Point out each malaria parasite.
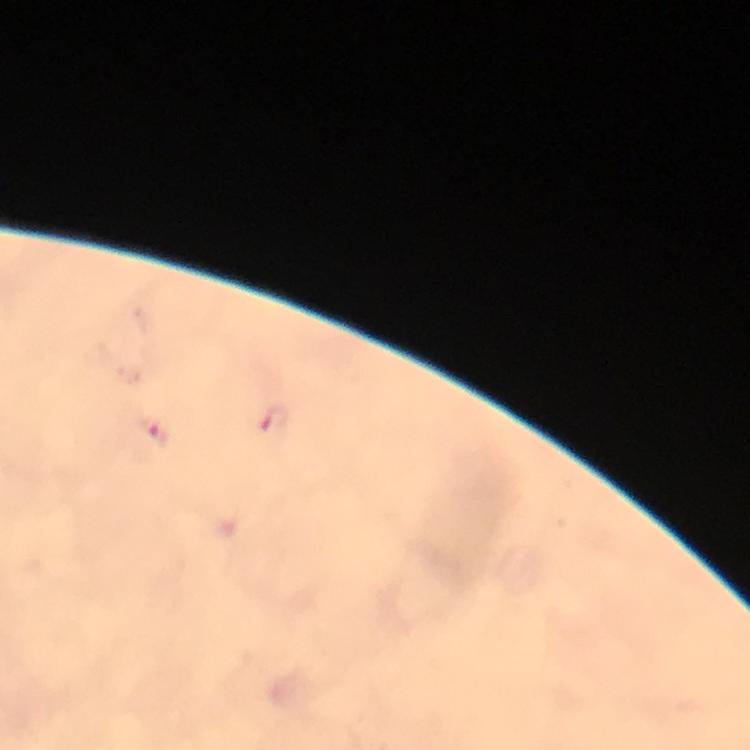
Approximate centers as (x, y) in pixels.
Malaria parasites: (272, 423), (154, 430).

Immersion oil applied. From a malaria diagnostic workup. Thick smear. Image is 750×750 pixels. Giemsa-stained preparation. 100x magnification. Cropped region of a single field of view. Smartphone photograph taken through a microscope.